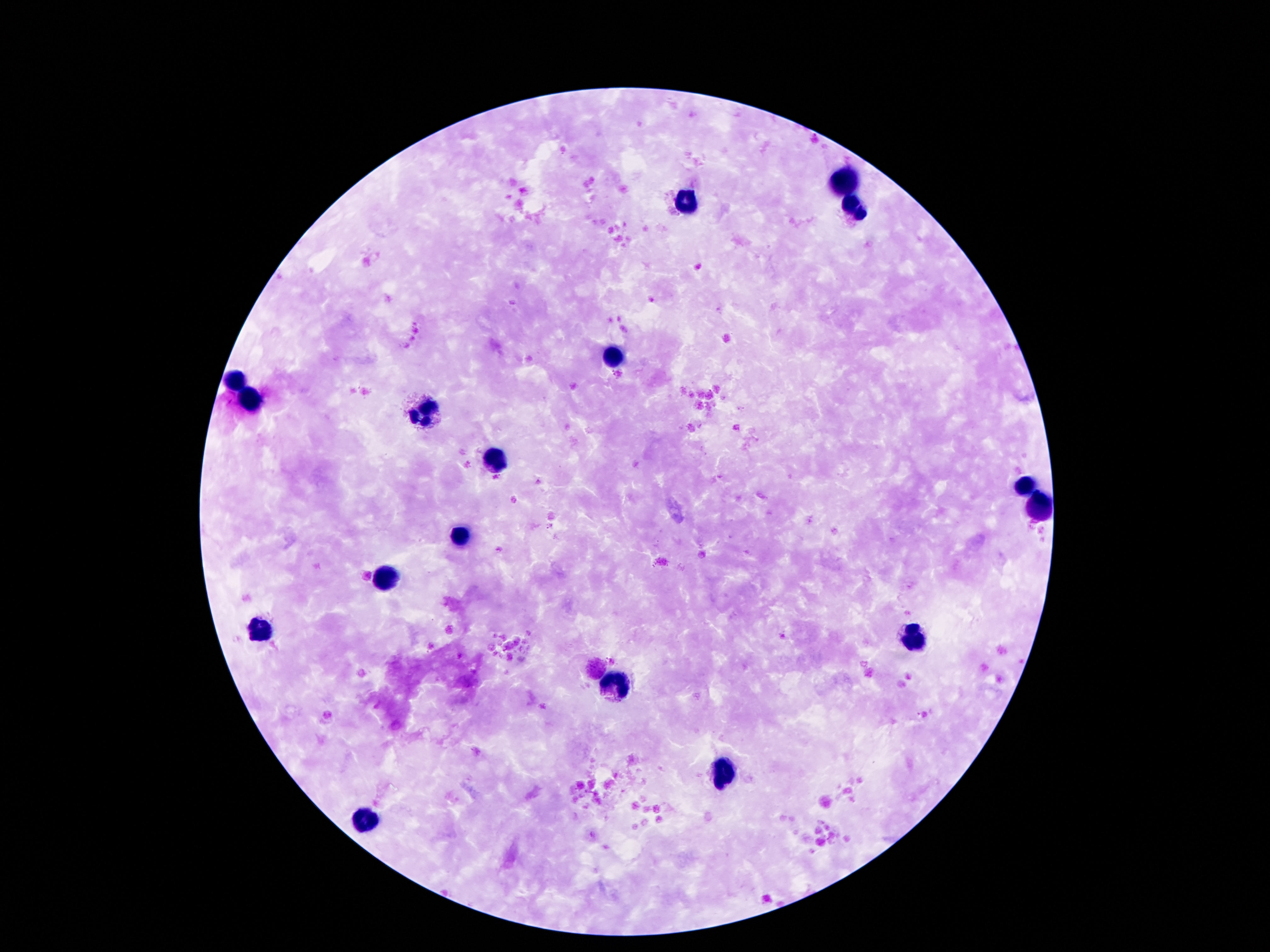

magnification: 100x
leukocyte_locations: 'approximate centers as (x, y) in pixels: (845, 179), (688, 205), (856, 213), (616, 354), (234, 385), (253, 402), (426, 414), (494, 461), (1026, 486), (1036, 508), (457, 539), (384, 581), (260, 632), (916, 637), (613, 683), (724, 774), (366, 820)'
image_size: 1270×952 pixels
patient_malaria_status: negative
stain: Giemsa
capture: smartphone camera through the microscope eyepiece
field_of_view: single
preparation: thick blood smear